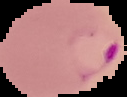 Malaria status: parasitized. Image is 127×97 pixels. From a thin blood smear. The area outside the segmented cell region is set to black.